Name the parasite shown.
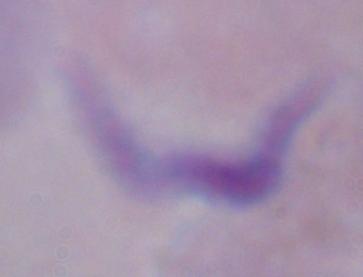
This is a trypanosome.

Summary:
  - Magnification: 1000x
  - Modality: micrograph